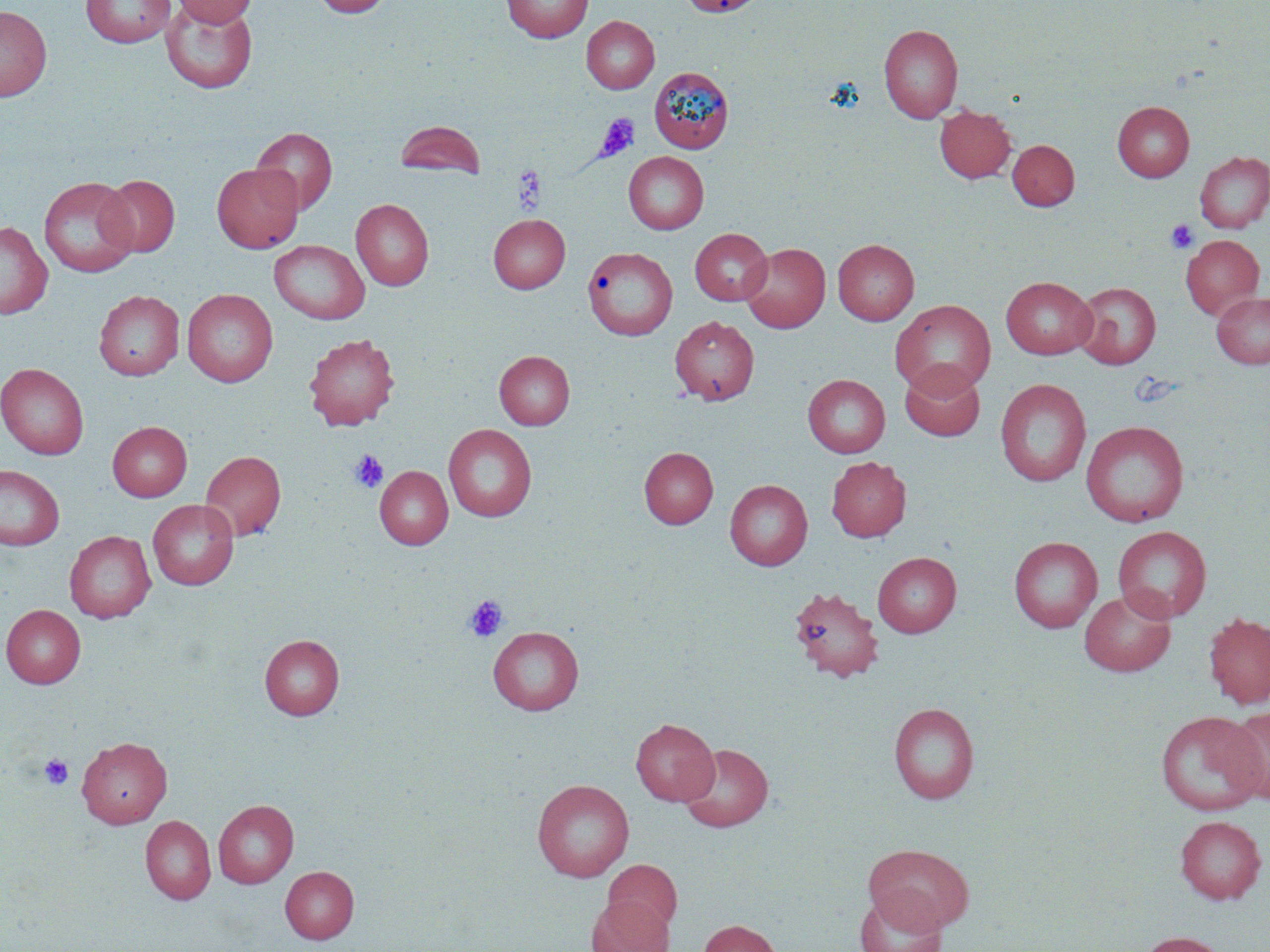

slide-level diagnosis = negative for blood parasites
stain = May-Grünwald-Giemsa
image size = 1270×952 pixels
uninfected red blood cell locations = approximate bounding boxes as [x1, y1, x2, y2] in pixels: [81, 0, 176, 48], [175, 0, 258, 27], [312, 0, 392, 17], [502, 0, 593, 42], [677, 0, 768, 18], [161, 2, 258, 94], [0, 4, 52, 101], [582, 16, 659, 93], [879, 24, 963, 123], [649, 67, 734, 153], [1112, 100, 1194, 182], [935, 104, 1016, 183], [395, 120, 485, 179], [251, 127, 338, 215], [1007, 140, 1079, 210], [1194, 151, 1270, 233], [623, 152, 709, 234], [211, 163, 303, 253], [99, 174, 180, 257], [39, 176, 139, 277], [351, 198, 433, 290], [488, 214, 570, 293], [0, 221, 52, 319], [690, 228, 772, 305], [1180, 234, 1264, 319], [833, 239, 919, 325], [269, 240, 369, 324], [740, 243, 830, 333], [582, 246, 676, 340], [1001, 276, 1096, 360], [1072, 282, 1160, 369], [182, 288, 278, 387], [94, 290, 184, 381], [1211, 291, 1270, 368], [891, 299, 996, 397], [670, 315, 759, 405], [304, 333, 400, 431], [494, 350, 575, 430], [0, 363, 89, 460], [899, 363, 985, 442], [803, 374, 890, 458], [995, 378, 1092, 486], [107, 421, 192, 501], [1081, 421, 1190, 527], [443, 424, 537, 522], [639, 447, 718, 529], [200, 449, 286, 541], [826, 456, 911, 542], [0, 464, 64, 550], [375, 465, 453, 550], [724, 480, 813, 570], [148, 499, 239, 590], [1113, 526, 1212, 623], [65, 530, 156, 623], [1009, 536, 1102, 632], [872, 552, 961, 637], [787, 586, 884, 682], [1079, 589, 1176, 677], [1, 604, 86, 688], [1203, 612, 1270, 709], [487, 626, 584, 716], [260, 633, 344, 720], [888, 702, 979, 804], [1223, 707, 1270, 804], [1154, 710, 1267, 815], [631, 718, 719, 805], [76, 736, 172, 828], [678, 743, 773, 832], [532, 779, 634, 881], [213, 799, 299, 888], [140, 815, 216, 904], [1174, 815, 1267, 904], [864, 843, 974, 933], [603, 859, 681, 933], [280, 866, 359, 943], [854, 889, 948, 952], [586, 895, 672, 952], [698, 919, 781, 952], [1135, 931, 1229, 952]
magnification = 1000x
platelet locations = approximate bounding boxes as [x1, y1, x2, y2] in pixels: [596, 113, 641, 160], [512, 165, 546, 212], [1165, 219, 1199, 254], [349, 450, 388, 493], [464, 595, 508, 642], [39, 754, 74, 790]
field of view = single
modality = light microscopy
preparation = thin blood smear